State which cell type is depicted.
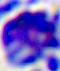

A leukocyte.

Captured at 400x magnification. Micrograph.